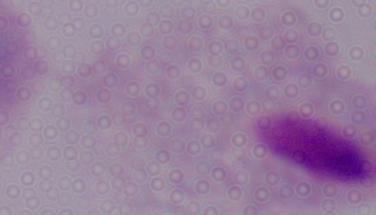

Summary:
  - Magnification: 1000x
  - Identification: trichomonad
  - Modality: photomicrograph